Describe the morphology of the red blood cells.
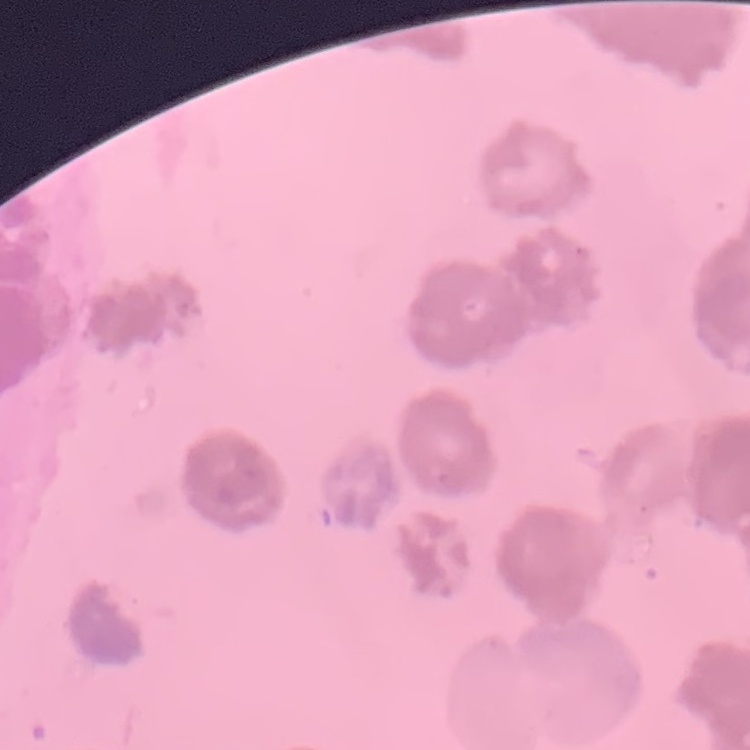

Rouleaux formation.

image type = one tile cut from a larger photomicrograph
preparation = thin peripheral smear
stain = Field's or Giemsa